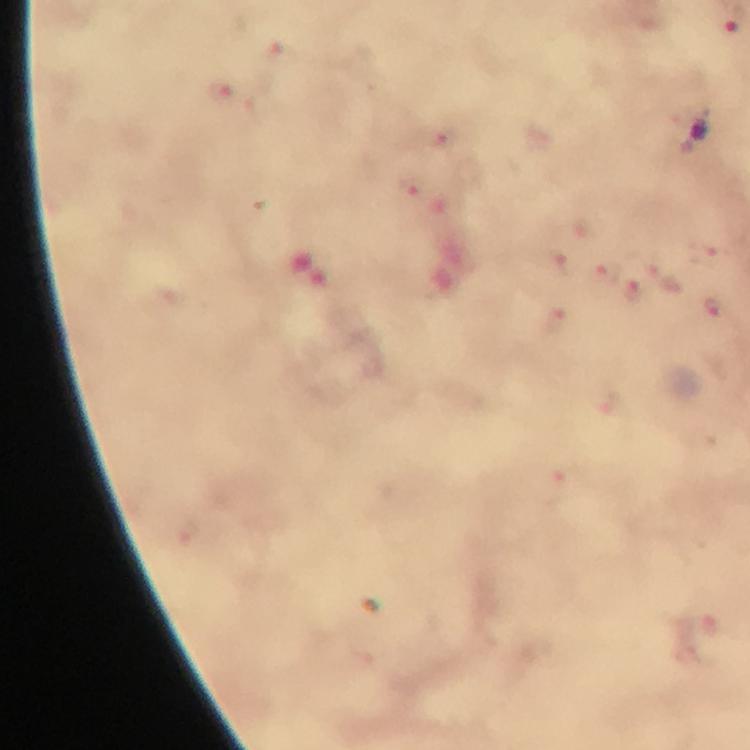 Approximate centers as [x, y] in pixels. Malaria parasite locations: [218, 90], [445, 135], [412, 188], [709, 256], [561, 259], [606, 272], [666, 278], [632, 291], [712, 313], [558, 319]. Smartphone photograph taken through a microscope. Giemsa-stained preparation. From a malaria diagnostic workup. Immersion oil applied. Cropped region of a single field of view. Image is 750×750 pixels. At 100x magnification. Thick blood film.